Point out every malaria parasite and every leukocyte.
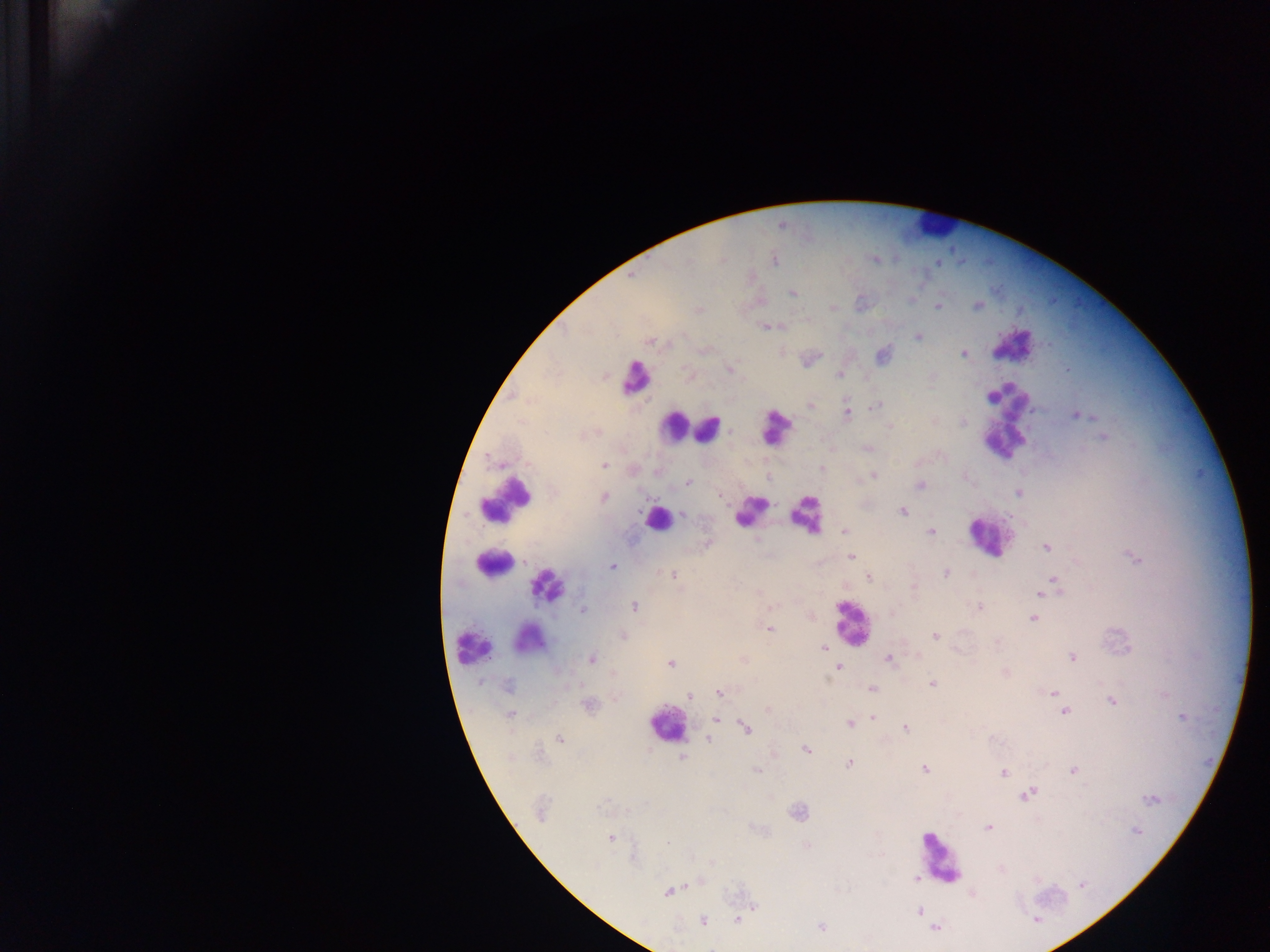
Approximate centers as x y in pixels.
Malaria parasites: 775 260; 633 275; 792 294; 912 300; 978 305; 938 306; 833 308; 699 310; 766 326; 918 337; 650 341; 963 354; 882 355; 730 370; 840 375; 811 405; 875 406; 847 413; 1079 416; 962 421; 889 427; 1103 437; 868 448; 605 465; 822 468; 873 476; 687 482; 920 484; 1019 492; 720 496; 603 498; 902 511; 682 514; 844 531; 931 532; 1046 547; 851 557; 1135 558; 613 566; 946 573; 673 575; 869 578; 1055 581; 914 587; 1049 587; 1041 593; 634 606; 979 606; 582 610; 1033 619; 770 629; 623 636; 935 636; 823 648; 1071 657; 591 659; 888 659; 670 664; 839 667; 1005 672; 932 684; 508 686; 872 689; 720 692; 1053 693; 690 697; 1112 702; 588 705; 768 709; 1064 712; 511 715; 873 717; 1182 717; 717 720; 854 722; 849 723; 746 728; 905 728; 559 738; 709 740; 806 749; 682 757; 849 764; 924 769; 1073 770; 758 771; 1003 771; 1027 794; 1151 799; 798 812; 987 827; 1137 831; 610 839; 668 842; 916 877; 1081 885; 668 891; 755 907; 919 911; 703 920; 737 920; 1036 920; 821 927; 935 928.
Leukocytes: 930 226; 1009 344; 636 378; 1008 399; 775 424; 675 427; 709 427; 1001 443; 506 499; 750 510; 806 514; 657 519; 988 537; 490 562; 547 586; 852 624; 526 641; 472 646; 666 725; 938 858.

Summary:
  - Country: Ghana
  - Image size: 1270×952 pixels
  - Field of view: single
  - Preparation: thick blood film
  - Capture: mobile-phone photograph through a microscope